Name the cell type shown.
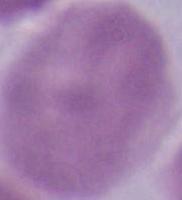
This is an erythrocyte.

{
  "magnification": "1000x",
  "modality": "micrograph"
}